Outline each Plasmodium falciparum parasite and classify it by life-cycle stage.
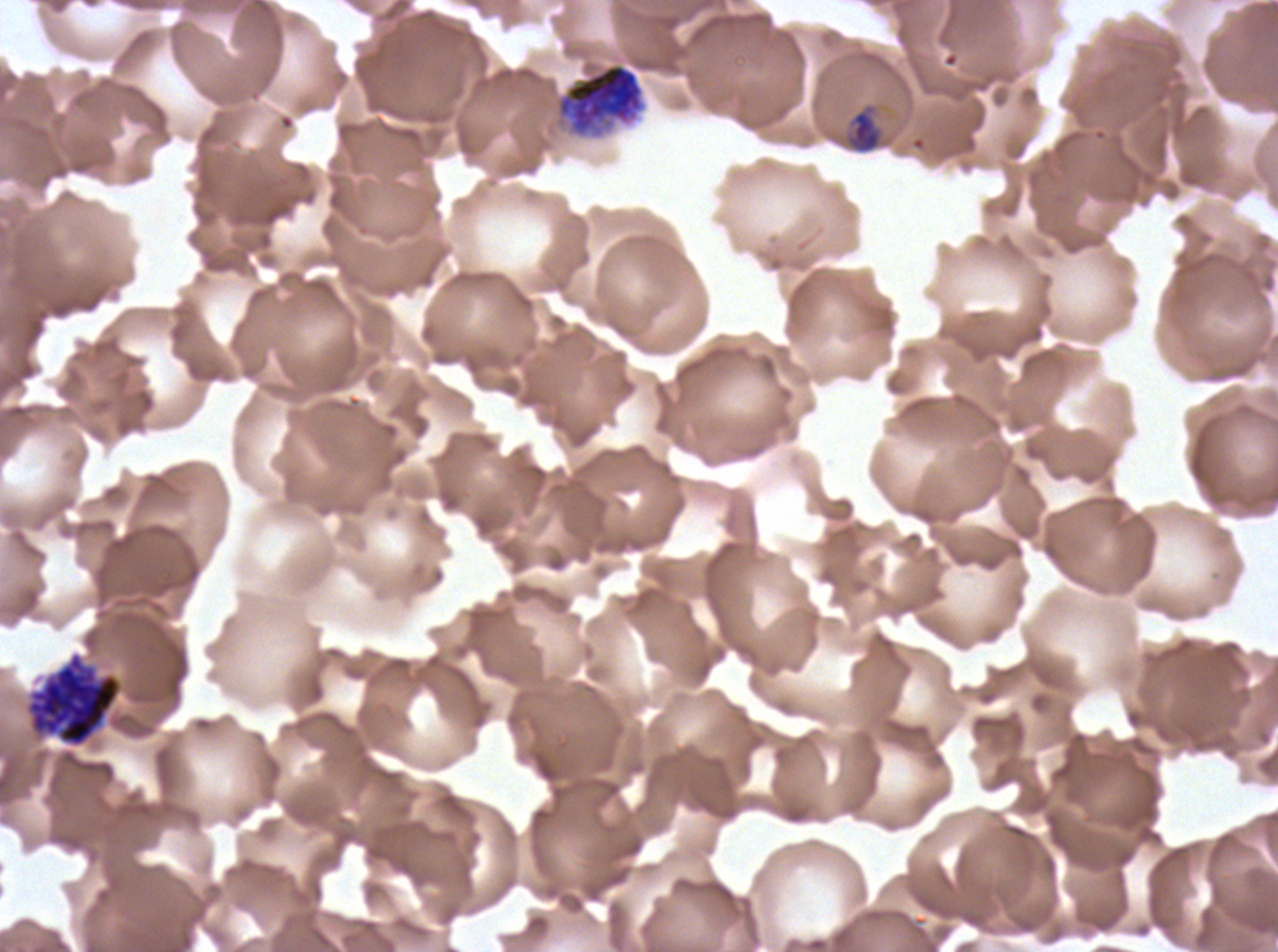
Approximate bounding boxes as [x1, y1, x2, y2] in pixels.
Late-ring/early-trophozoite forms: [845, 104, 883, 154].
Segmenters: [555, 62, 646, 139], [27, 653, 121, 747].
No rings, mid trophozoites, late trophozoites, early schizonts, late schizonts, or gametocytes observed.

field_of_view: sub-image separated from a larger composite
preparation: thin blood film
specimen: Plasmodium falciparum cultured ex vivo for 24 to 48 hours, from a patient in The Gambia
stain: Giemsa
image_size: 1278×952 pixels
life_cycle_stages_observed: late-ring/early-trophozoite, segmenter